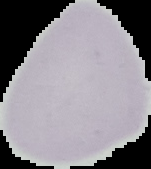
Summary:
  - Image type: segmented cell region on a black background
  - Image size: 151×169 pixels
  - Preparation: thin blood film
  - Malaria status: uninfected